State which parasite is depicted.
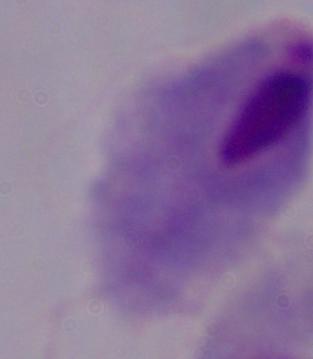
This is a trichomonad.

Summary:
  - Modality: micrograph
  - Magnification: 1000x